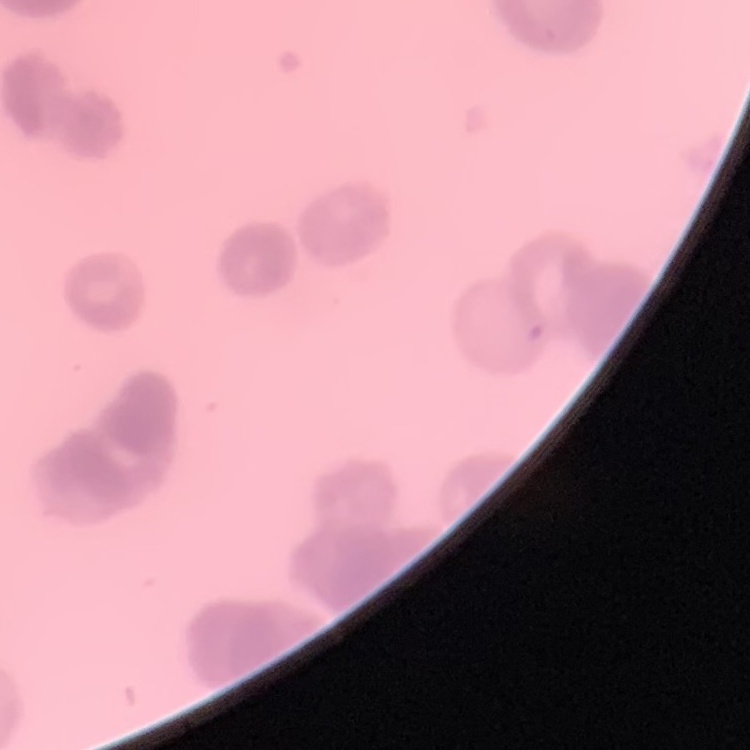

red blood cell morphology = rouleaux formation
stain = Field's or Giemsa
image type = one tile cut from a larger photomicrograph
preparation = thin peripheral smear